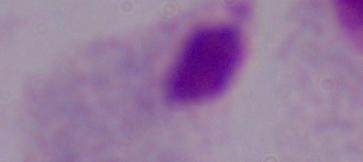

A trichomonad is seen. Micrograph. 1000x magnification.